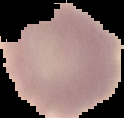
{
  "image_size": "124×118 pixels",
  "result": "no Plasmodium parasites seen",
  "preparation": "thin blood film",
  "image_type": "cell region segmented out of the field of view; surrounding area masked to black"
}